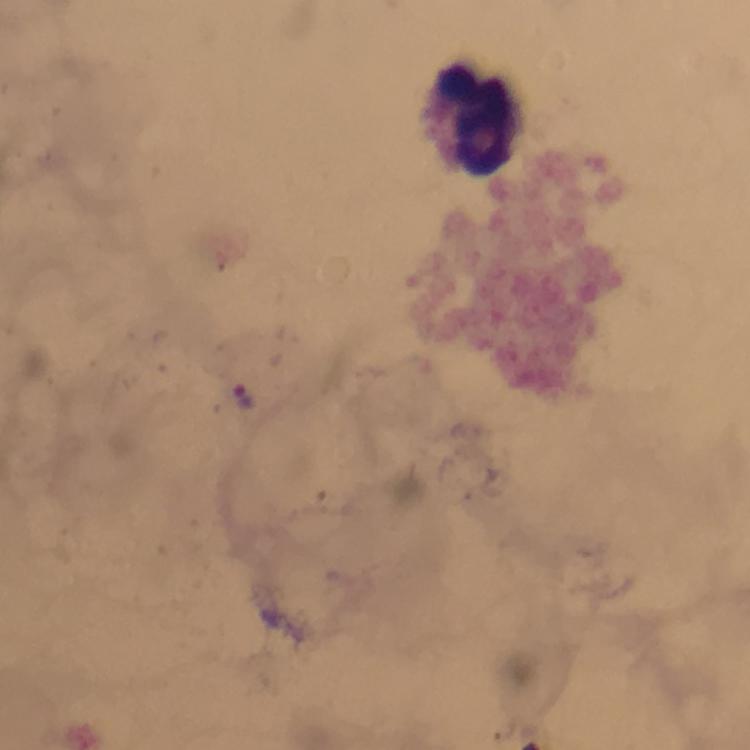

Approximate object centers, in pixels from the top-left corner.
Summary:
  - Plasmodium parasite locations: (x=243, y=395)
  - Leukocyte locations: (x=468, y=118)
  - Stain: Giemsa
  - Image size: 750×750 pixels
  - Magnification: 100x
  - Context: from a malaria diagnostic workup
  - Preparation: thick blood film
  - Immersion oil: applied
  - Cropped from: one field of view
  - Capture: smartphone mounted on the microscope